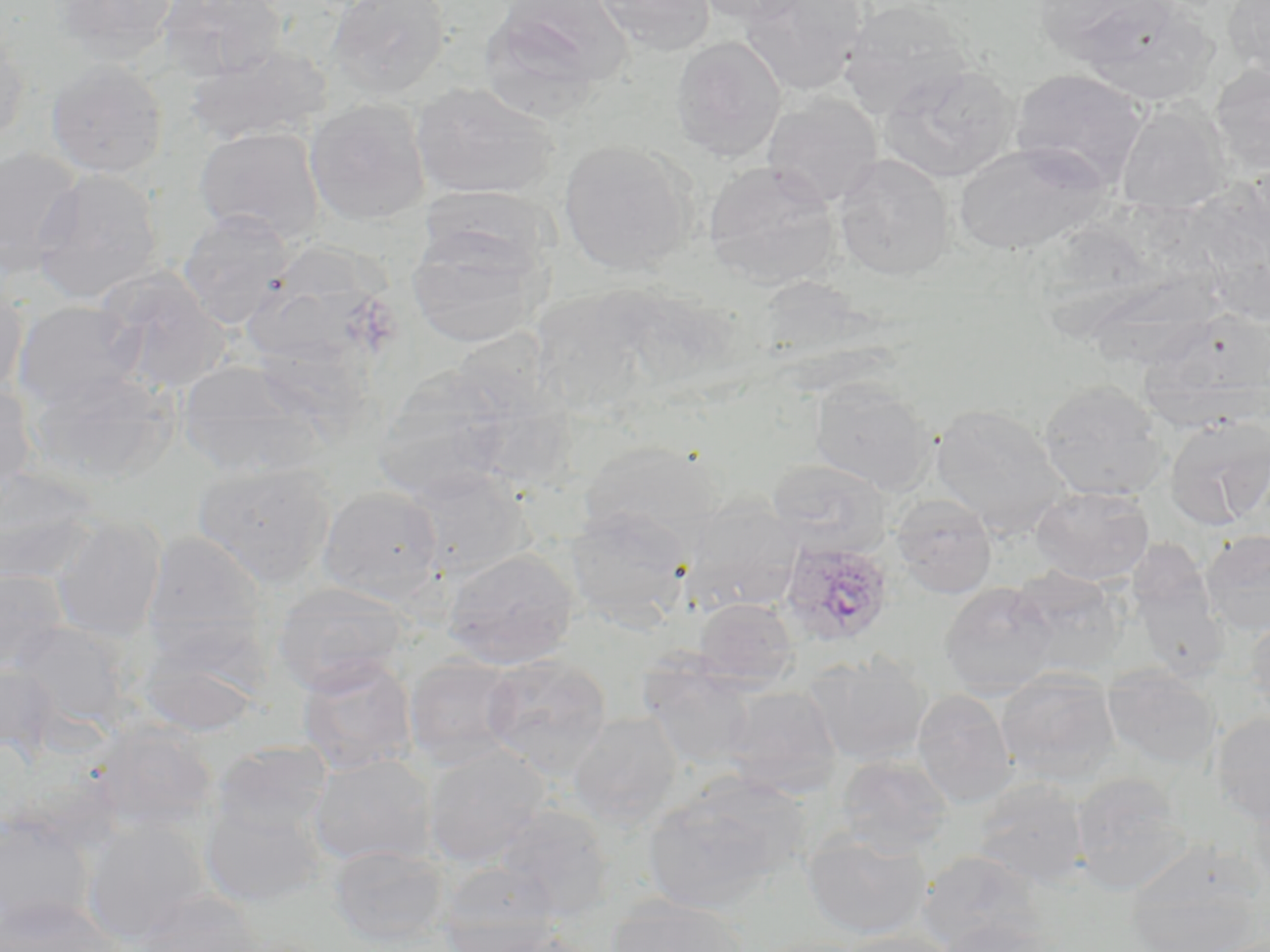
Summary:
  - Coordinate format: approximate bounding boxes as (x1,y1)-(x2,y2) corner pairs in pixels
  - Plasmodium ovale-infected red blood cell locations: (779,539)-(895,648)
  - Uninfected red blood cell locations: (52,0)-(180,64), (158,0)-(284,81), (326,0)-(452,99), (481,0)-(632,114), (593,0)-(716,57), (692,0)-(811,25), (740,0)-(868,95), (838,0)-(974,119), (1035,0)-(1173,64), (1223,0)-(1270,80), (1081,6)-(1218,105), (0,27)-(30,147), (670,36)-(787,163), (184,44)-(332,147), (46,59)-(167,178), (879,64)-(1019,184), (1210,65)-(1270,174), (1011,69)-(1146,188), (411,82)-(559,201), (763,93)-(883,207), (305,98)-(430,226), (1116,102)-(1229,213), (194,126)-(325,244), (558,140)-(696,276), (953,141)-(1110,254), (0,146)-(84,277), (833,154)-(955,281), (702,160)-(841,288), (32,168)-(164,304), (177,209)-(293,328), (407,225)-(544,349), (257,240)-(388,358), (96,270)-(230,396), (0,274)-(29,400), (535,286)-(670,407), (12,299)-(144,411), (1150,312)-(1270,427), (177,361)-(325,480), (371,366)-(518,503), (28,369)-(177,486), (808,378)-(936,495), (1038,379)-(1169,502), (0,380)-(39,497), (930,403)-(1070,538), (1165,414)-(1270,530), (578,439)-(725,552), (766,457)-(894,558), (191,460)-(339,588), (0,467)-(96,584), (405,468)-(532,581), (1031,485)-(1154,586), (317,486)-(444,604), (891,493)-(997,598), (679,496)-(803,614), (564,507)-(693,630), (51,514)-(168,640), (141,529)-(267,653), (1200,529)-(1270,636), (443,548)-(579,669), (1010,567)-(1127,678), (0,569)-(67,676), (1131,570)-(1230,684), (270,581)-(409,695), (939,582)-(1059,697), (693,597)-(798,687), (1244,614)-(1270,720), (8,620)-(133,729), (132,621)-(268,736), (481,652)-(613,775), (807,652)-(933,766), (297,656)-(418,776), (404,656)-(520,770), (639,661)-(758,769), (0,663)-(62,764), (1102,665)-(1222,769), (996,668)-(1121,784), (723,684)-(842,797), (912,689)-(1018,809), (1211,711)-(1270,825), (568,712)-(683,829), (85,720)-(221,835), (210,741)-(333,837), (423,745)-(550,866), (308,754)-(436,867), (835,754)-(954,858), (1071,772)-(1192,894), (971,777)-(1090,888), (642,779)-(802,915), (1246,793)-(1270,899), (199,795)-(328,908), (494,806)-(614,919), (0,812)-(97,934), (81,820)-(212,945), (801,830)-(931,940), (328,845)-(452,948), (917,850)-(1046,952), (1124,859)-(1266,952), (435,861)-(562,951), (130,890)-(264,952), (0,896)-(127,952), (606,898)-(749,952), (935,916)-(1062,952), (443,921)-(579,952), (834,929)-(963,952), (748,936)-(875,952)
  - Slide-level diagnosis: Plasmodium ovale
  - Stain: May-Grünwald-Giemsa
  - Modality: optical microscopy
  - Field of view: single
  - Preparation: thin blood smear
  - Magnification: 1000x
  - Image size: 1270×952 pixels